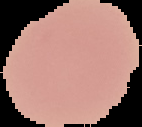

Summary:
  - Preparation: thin blood film
  - Image size: 142×127 pixels
  - Malaria status: uninfected
  - Image type: segmented cell region with the area outside set to black